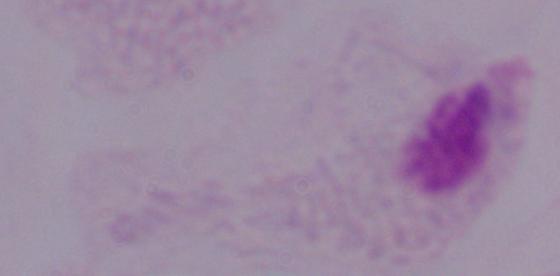
modality: photomicrograph
identification: trichomonad
magnification: 1000x